Report the malaria status of this cell.
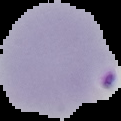
It is parasitized.

Image is 121×121 pixels. From a thin blood smear. Segmented cell region on a black background.